Point out leukocytes.
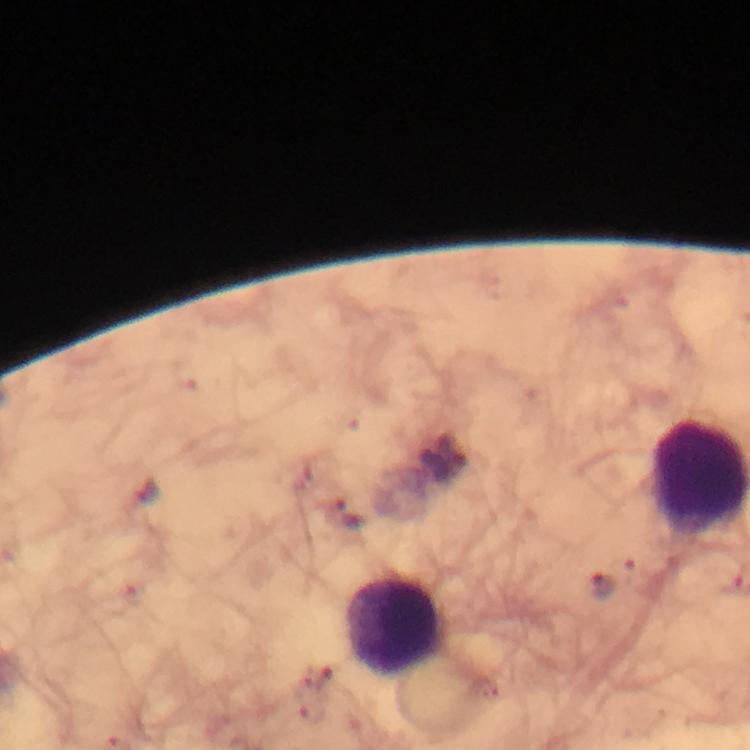

Approximate centers as [x, y] in pixels.
Leukocytes: [395, 626].

Summary:
  - Plasmodium parasite locations: [452, 450], [347, 514], [601, 584]
  - Immersion oil: applied
  - Capture: smartphone camera through the microscope
  - Preparation: thick blood smear
  - Stain: Giemsa
  - Magnification: 100x
  - Cropped from: a single field of view
  - Context: from a malaria diagnostic workup
  - Image size: 750×750 pixels